Outline each blood parasite and name the species.
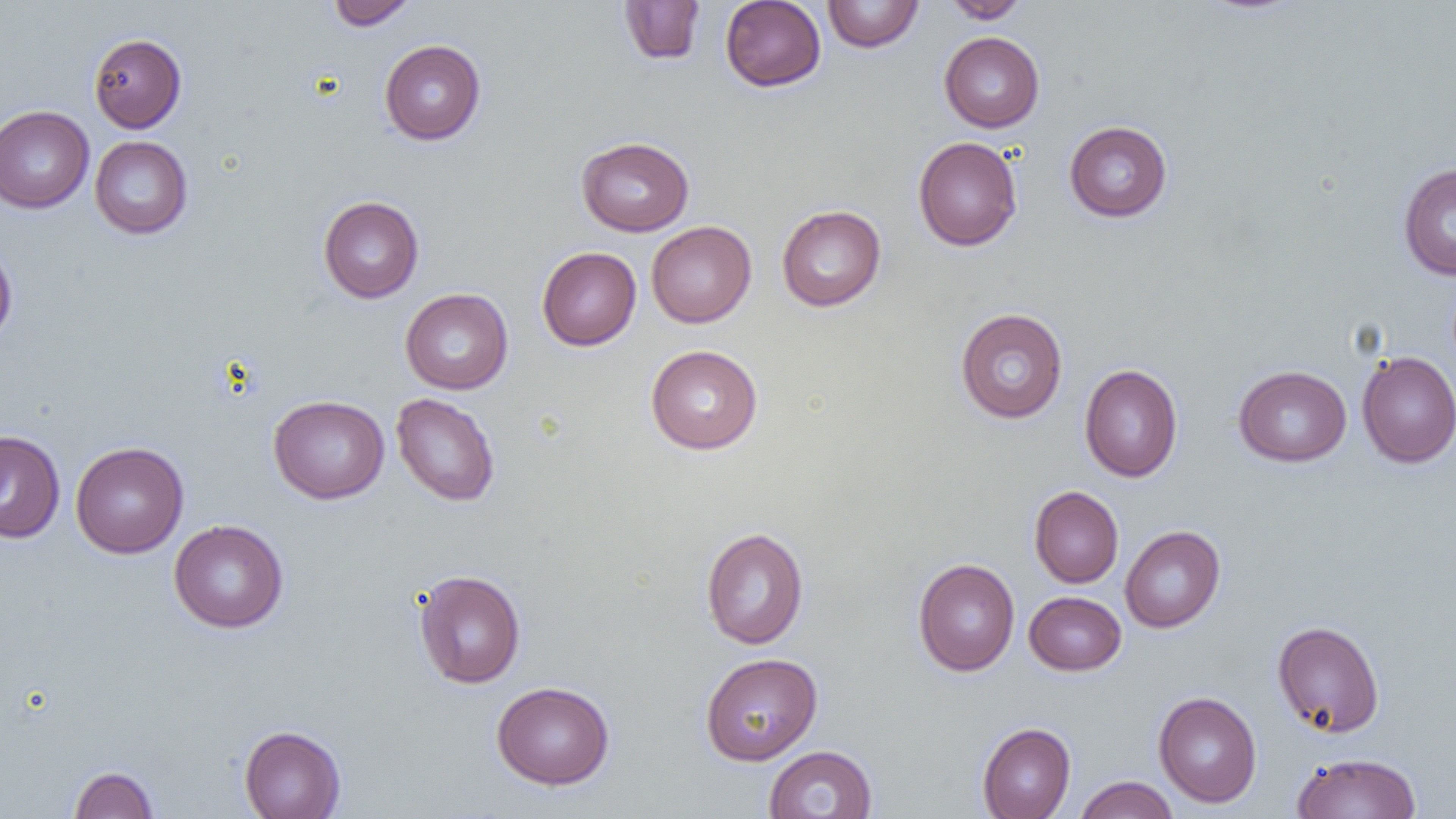

No blood parasites observed.

{
  "slide_level_diagnosis": "negative for blood parasites",
  "modality": "light microscopy",
  "uninfected_red_blood_cell_locations": "approximate bounding boxes as (x1, y1, x2, y2) in pixels: (328, 0, 418, 29), (941, 0, 1030, 23), (619, 1, 705, 66), (720, 1, 826, 92), (822, 1, 924, 52), (939, 32, 1044, 132), (88, 33, 187, 132), (379, 39, 486, 145), (0, 105, 94, 214), (1064, 120, 1172, 222), (89, 136, 193, 239), (576, 136, 694, 236), (913, 136, 1023, 251), (1397, 163, 1456, 280), (318, 196, 424, 303), (776, 204, 886, 311), (646, 221, 757, 327), (0, 239, 18, 345), (537, 247, 641, 350), (400, 288, 513, 394), (955, 308, 1068, 423), (645, 344, 763, 454), (1356, 351, 1456, 467), (1079, 364, 1183, 482), (1233, 365, 1351, 466), (390, 392, 501, 507), (268, 395, 389, 504), (0, 430, 65, 543), (70, 441, 188, 558), (1029, 486, 1123, 588), (169, 519, 289, 633), (1120, 525, 1225, 632), (701, 527, 809, 650), (912, 558, 1020, 676), (413, 570, 526, 689), (1024, 591, 1126, 675), (1272, 620, 1385, 737), (699, 652, 823, 765), (491, 681, 615, 790), (1153, 691, 1262, 807), (976, 722, 1076, 819), (238, 725, 346, 819), (763, 745, 878, 819), (1292, 752, 1422, 818), (69, 765, 159, 819), (1074, 776, 1179, 819)",
  "preparation": "thin blood smear",
  "field_of_view": "one of a larger specimen",
  "image_size": "1456×819 pixels",
  "magnification": "1000x"
}